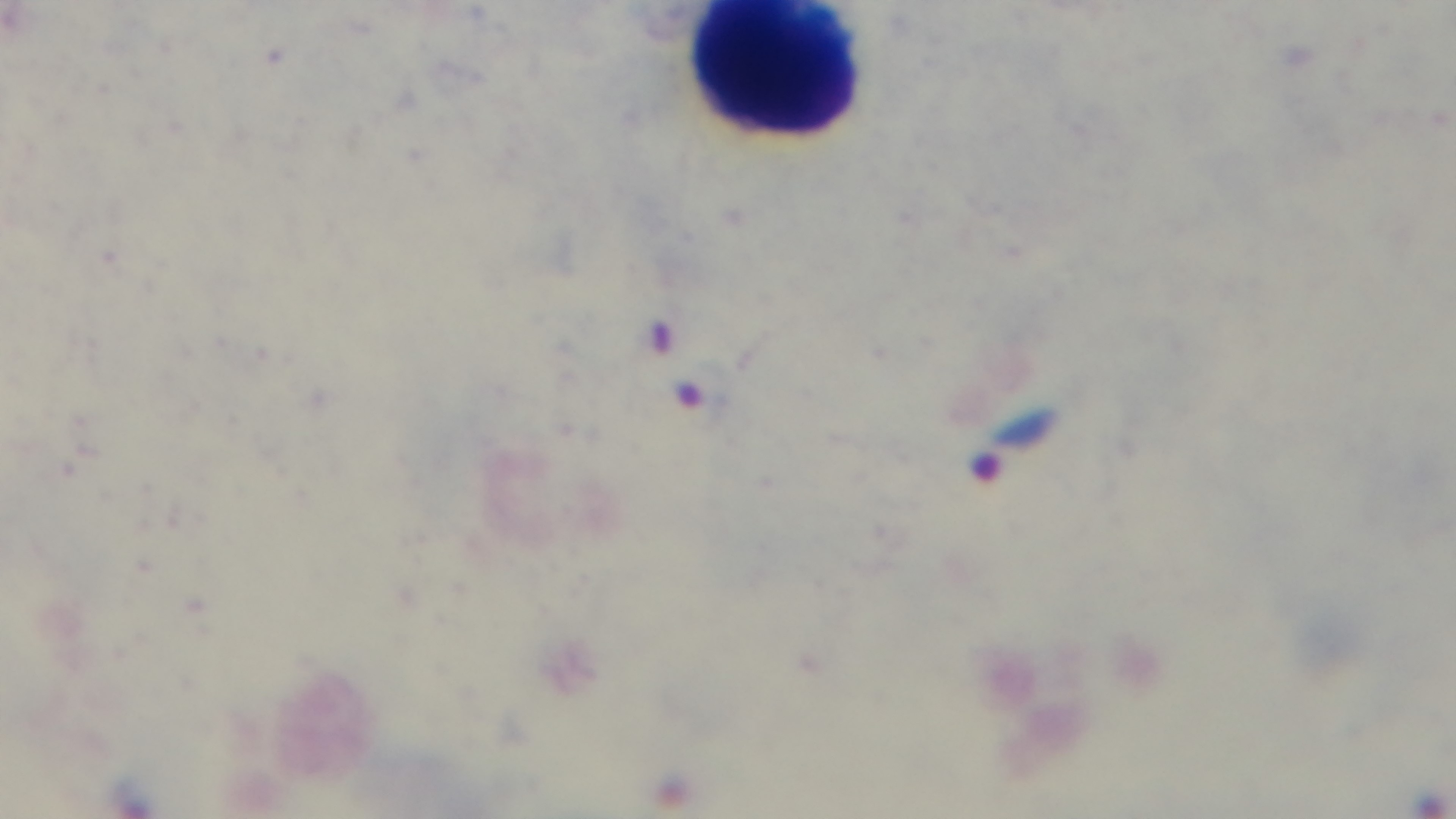
Malaria status: infected. 100x oil-immersion objective. Preparation: thick blood film. Mounted 4K digital camera. Single field of view. Giemsa-stained. Photomicrograph.